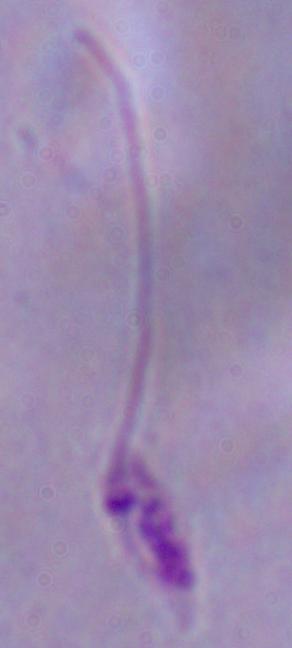

Summary:
  - Magnification: 1000x
  - Identification: Leishmania
  - Modality: photomicrograph